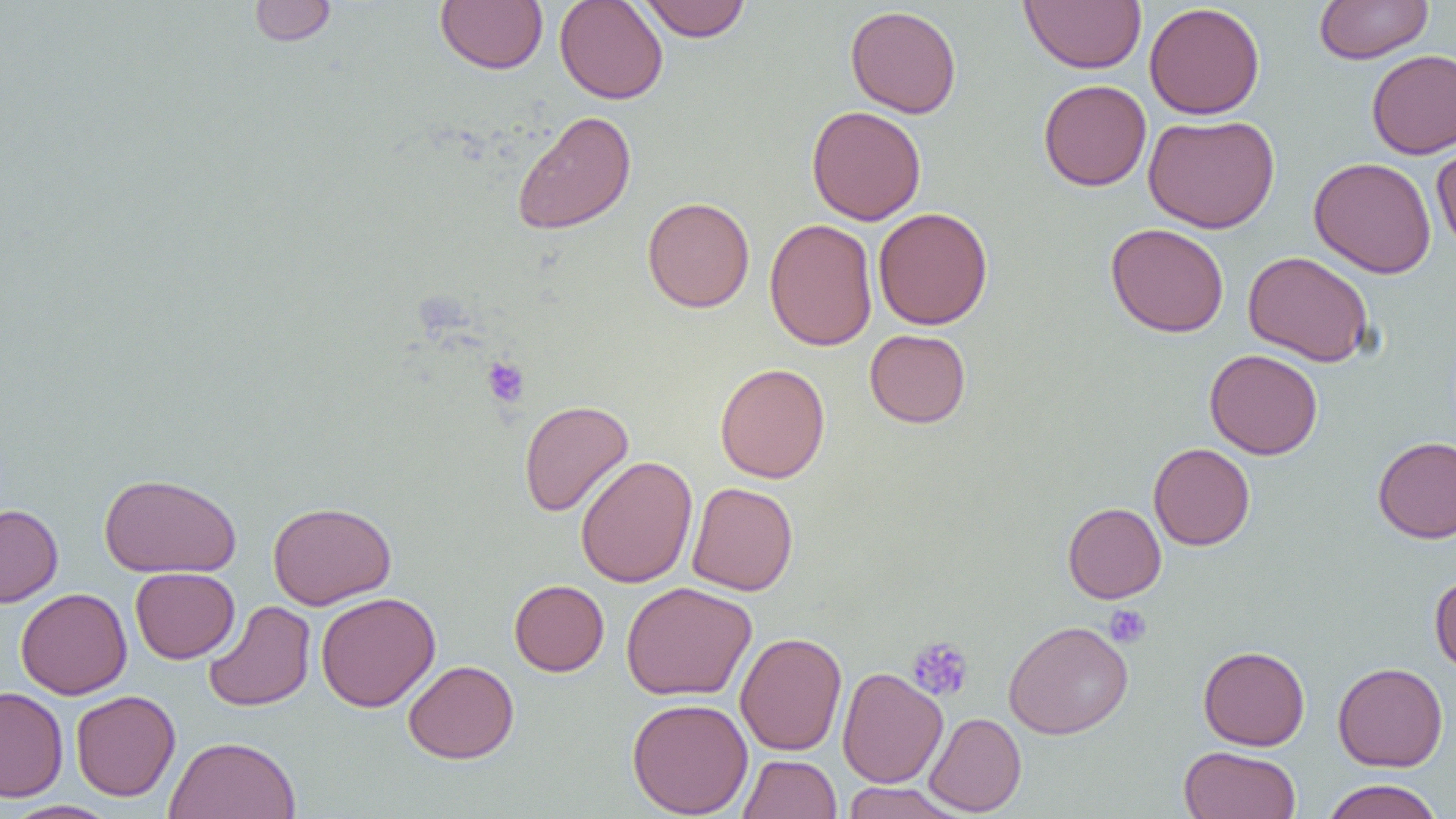
Approximate bounding boxes as [x1, y1, x2, y2] in pixels. Platelet locations: [481, 356, 530, 408], [1104, 604, 1152, 649], [906, 636, 974, 702]. Uninfected red blood cell locations: [248, 0, 336, 46], [554, 0, 668, 104], [638, 0, 751, 42], [1315, 0, 1433, 64], [435, 1, 548, 74], [1020, 1, 1146, 73], [1144, 2, 1265, 120], [845, 5, 962, 118], [1366, 49, 1456, 158], [1038, 79, 1152, 191], [806, 105, 926, 225], [512, 110, 636, 235], [1142, 113, 1280, 233], [1432, 140, 1456, 256], [1308, 157, 1437, 279], [642, 196, 755, 313], [873, 207, 993, 330], [764, 218, 878, 352], [1105, 223, 1229, 337], [1243, 250, 1374, 367], [864, 329, 971, 428], [1205, 348, 1323, 460], [715, 362, 830, 484], [519, 399, 634, 517], [1372, 436, 1456, 544], [1148, 443, 1255, 550], [574, 456, 698, 587], [98, 473, 241, 577], [687, 482, 798, 596], [267, 501, 396, 609], [1062, 502, 1166, 603], [0, 504, 63, 607], [130, 567, 240, 663], [1429, 573, 1456, 675], [509, 579, 610, 676], [621, 582, 757, 701], [15, 588, 132, 699], [316, 592, 440, 712], [203, 600, 316, 712], [1003, 620, 1133, 739], [735, 632, 847, 755], [1198, 645, 1310, 751], [403, 660, 520, 764], [1333, 661, 1448, 771], [837, 667, 948, 788], [0, 687, 68, 802], [70, 690, 180, 801], [626, 697, 753, 818], [924, 712, 1026, 816], [164, 735, 302, 819], [1179, 745, 1302, 819], [738, 754, 842, 818], [1321, 779, 1444, 819], [840, 782, 967, 819], [2, 800, 120, 819]. Slide-level diagnosis: no evidence of blood parasites. 1000x magnification. One field of a larger specimen. Thin blood film. Optical microscopy. Image is 1456×819 pixels.